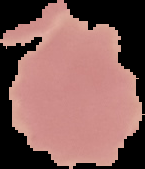
image type = cell region segmented out of the field of view; surrounding area masked to black
malaria status = uninfected
preparation = thin blood film
image size = 145×169 pixels